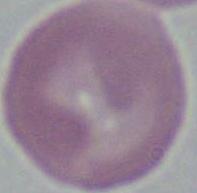

Summary:
  - Modality: micrograph
  - Identification: erythrocyte
  - Magnification: 1000x